Outline each uninfected red blood cell.
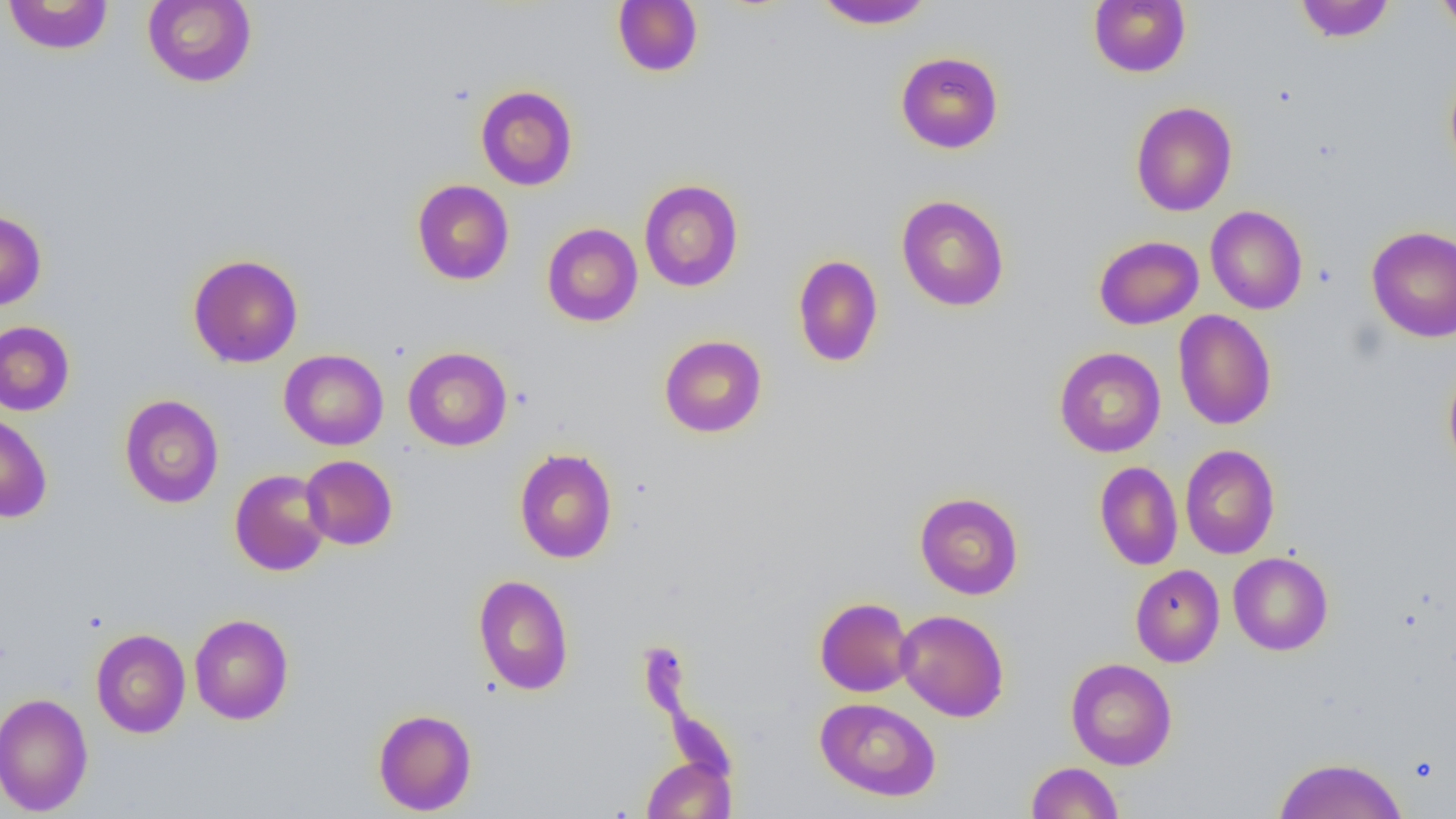

Approximate bounding boxes as (x1, y1, x2, y2) in pixels.
Uninfected red blood cells: (142, 0, 258, 88), (612, 0, 704, 77), (1088, 0, 1190, 77), (1294, 0, 1396, 43), (1435, 0, 1456, 35), (2, 1, 114, 56), (814, 1, 935, 30), (895, 51, 1004, 154), (1444, 67, 1456, 185), (476, 85, 578, 190), (1130, 101, 1238, 217), (412, 179, 514, 285), (639, 179, 744, 292), (896, 195, 1010, 312), (1205, 205, 1308, 314), (0, 210, 47, 310), (541, 222, 643, 327), (1366, 226, 1456, 342), (1093, 235, 1204, 330), (188, 253, 303, 368), (792, 255, 884, 367), (1173, 309, 1276, 430), (0, 320, 75, 416), (659, 334, 767, 438), (402, 346, 513, 451), (1054, 346, 1166, 457), (279, 349, 389, 450), (1443, 362, 1456, 476), (119, 394, 224, 509), (0, 411, 53, 523), (1180, 444, 1280, 559), (513, 447, 618, 563), (300, 455, 398, 550), (1094, 461, 1183, 570), (230, 468, 331, 576), (914, 492, 1024, 599), (1228, 551, 1333, 655), (1130, 564, 1225, 667), (473, 575, 574, 695), (814, 597, 916, 698), (895, 609, 1009, 721), (189, 613, 294, 724), (91, 628, 191, 738), (1066, 657, 1177, 770), (0, 692, 94, 816), (815, 697, 941, 801), (373, 709, 477, 816), (641, 756, 736, 818), (1273, 756, 1409, 819), (1025, 762, 1124, 818).

{
  "slide_level_diagnosis": "negative for blood parasites",
  "magnification": "1000x",
  "modality": "light microscopy",
  "preparation": "thin blood film",
  "image_size": "1456×819 pixels",
  "field_of_view": "one of a larger specimen"
}